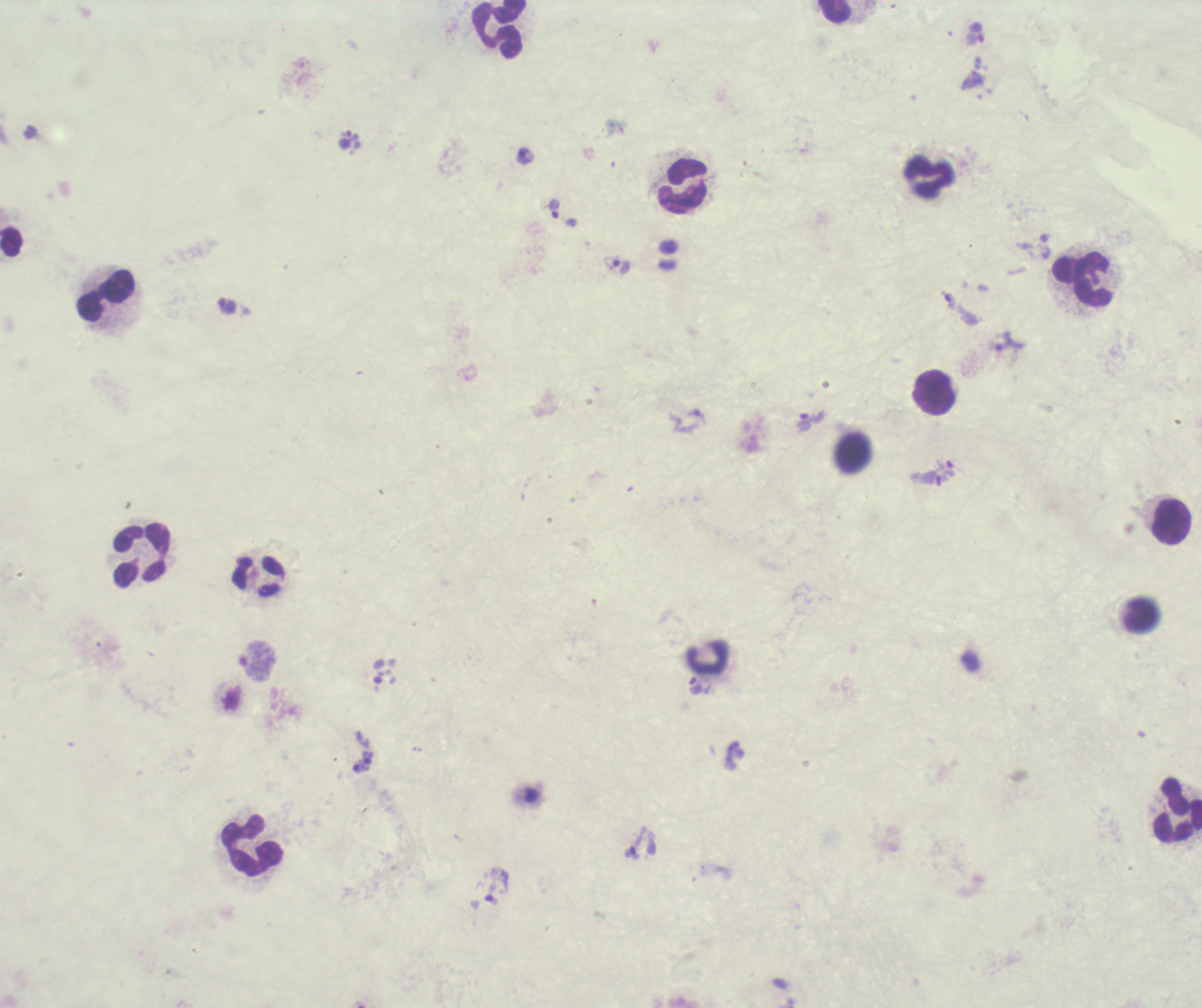
{
  "trophozoite_locations": "approximate centers as [x, y] in pixels: [974, 33], [972, 81], [345, 140], [525, 156], [554, 209], [621, 266], [950, 301], [227, 306], [696, 416], [810, 421], [949, 469], [932, 478], [695, 687], [735, 754], [367, 757], [361, 767], [633, 853], [492, 896]",
  "context": "previously used in a real diagnosis",
  "field_of_view": "one from this slide",
  "preparation": "thick smear of blood",
  "background_quality": "unsatisfactory",
  "magnification": "100x",
  "result": "Plasmodium parasites detected",
  "coloration_quality": "bad",
  "image_size": "1202×1008 pixels",
  "leukocyte_locations": "approximate centers as [x, y] in pixels: [833, 11], [500, 30], [928, 177], [681, 186], [1083, 281], [104, 295], [933, 392], [854, 453], [1171, 521], [141, 556], [258, 575], [1142, 615], [708, 658], [1177, 810], [253, 846]",
  "stain": "Romanowsky"
}